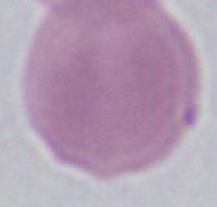
Summary:
  - Modality: photomicrograph
  - Identification: erythrocyte
  - Magnification: 1000x